Classify this cell by malaria status.
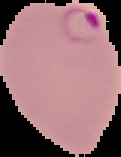
It is parasitized.

{
  "preparation": "thin blood smear",
  "image_type": "segmented cell region with the area outside set to black",
  "image_size": "121×157 pixels"
}